Outline each blood parasite and name the species.
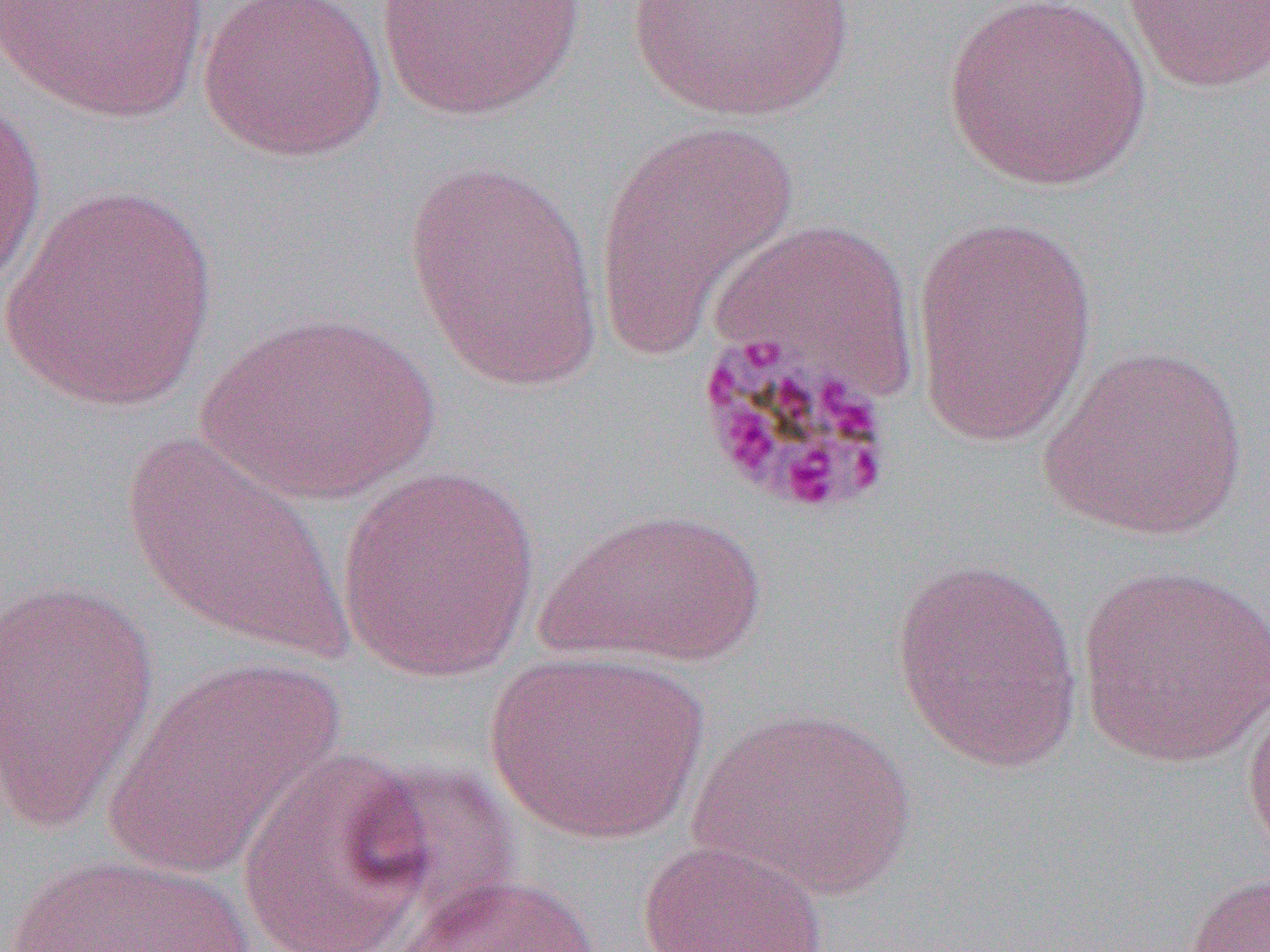
Approximate bounding boxes as named x1/y1/x2/y2 corners in pixels.
Plasmodium malariae-infected red blood cells: (x1=690, y1=330, x2=897, y2=519).
No Plasmodium falciparum, Plasmodium ovale, Plasmodium vivax, Babesia divergens, or Trypanosoma brucei observed.

Uninfected red blood cell locations: (x1=0, y1=0, x2=210, y2=123), (x1=196, y1=0, x2=389, y2=164), (x1=626, y1=0, x2=857, y2=125), (x1=942, y1=0, x2=1151, y2=191), (x1=1122, y1=0, x2=1270, y2=94), (x1=373, y1=1, x2=586, y2=121), (x1=0, y1=93, x2=49, y2=295), (x1=594, y1=121, x2=799, y2=355), (x1=401, y1=158, x2=604, y2=390), (x1=1, y1=184, x2=217, y2=412), (x1=910, y1=215, x2=1100, y2=447), (x1=709, y1=216, x2=920, y2=405), (x1=196, y1=311, x2=442, y2=506), (x1=1038, y1=342, x2=1250, y2=543), (x1=121, y1=429, x2=351, y2=662), (x1=335, y1=464, x2=543, y2=684), (x1=539, y1=506, x2=766, y2=667), (x1=890, y1=558, x2=1085, y2=773), (x1=1076, y1=564, x2=1270, y2=768), (x1=0, y1=578, x2=161, y2=835), (x1=485, y1=649, x2=707, y2=845), (x1=101, y1=655, x2=346, y2=882), (x1=1241, y1=692, x2=1270, y2=869), (x1=689, y1=706, x2=919, y2=900), (x1=234, y1=747, x2=444, y2=952), (x1=636, y1=838, x2=831, y2=951), (x1=3, y1=851, x2=261, y2=952), (x1=1183, y1=870, x2=1269, y2=952), (x1=392, y1=872, x2=606, y2=952). Slide-level diagnosis: Plasmodium malariae. Thin blood smear. 1000x magnification. Optical microscopy. Image is 1270×952 pixels. One field of a larger specimen.